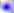
Toxoplasma gondii is seen. Captured at 400x magnification. Micrograph.